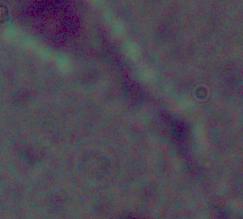

Summary:
  - Modality: micrograph
  - Identification: Leishmania
  - Magnification: 1000x